State which cell type is depicted.
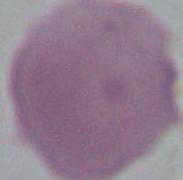

This is an erythrocyte.

{
  "modality": "photomicrograph",
  "magnification": "1000x"
}